Describe the morphology of the erythrocytes.
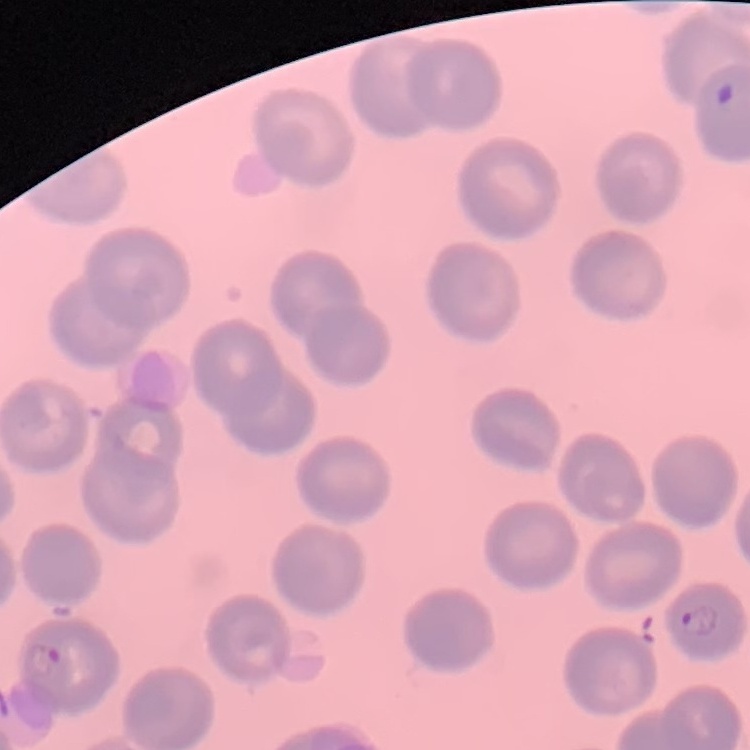
They show no rouleaux formation.

Summary:
  - Preparation: thin blood smear
  - Stain: Field's or Giemsa
  - Image type: square crop of a larger photomicrograph